Point out each leukocyte.
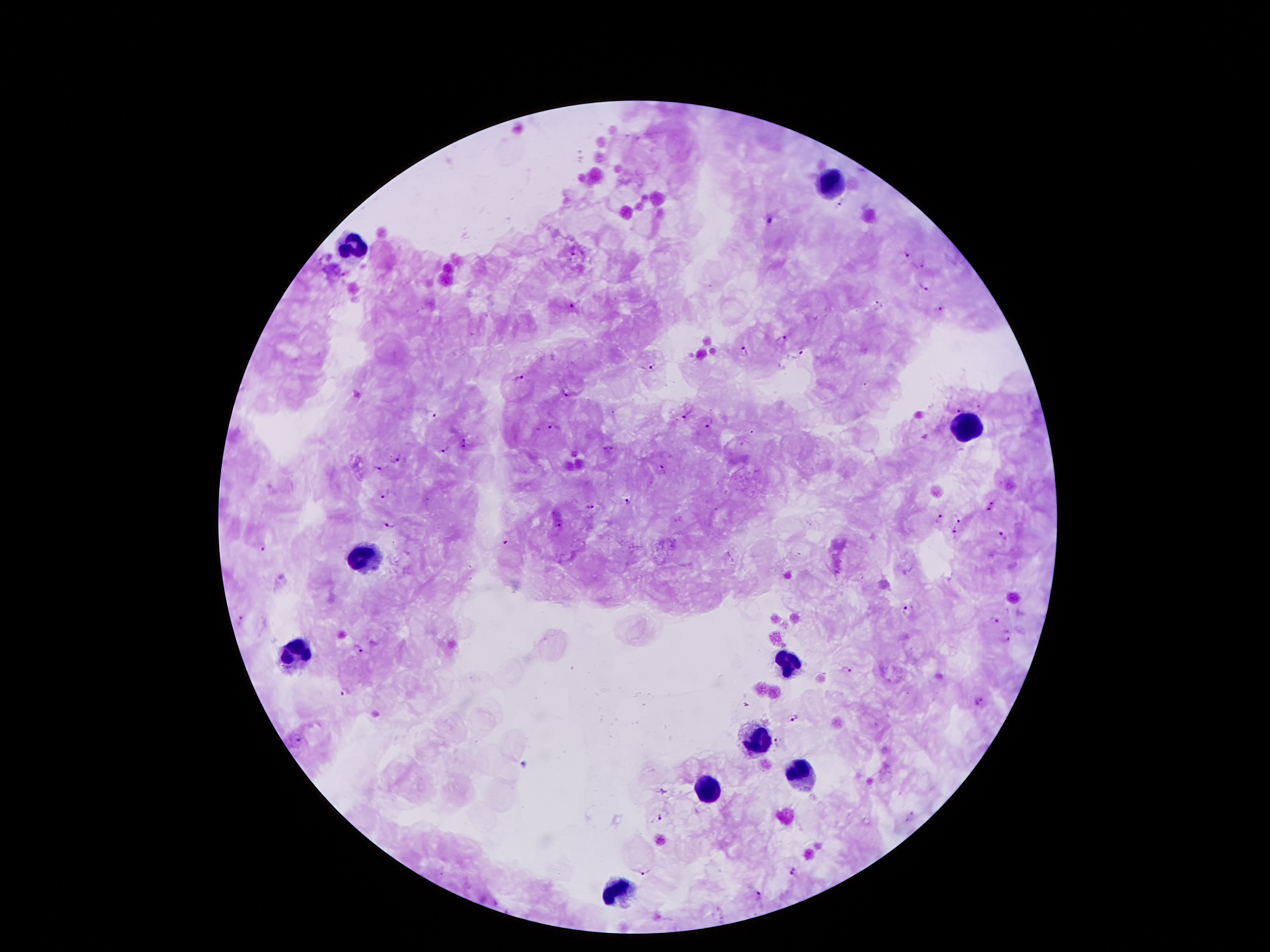
Approximate object centers, in pixels from the top-left corner.
Leukocytes: (x=830, y=181), (x=347, y=246), (x=965, y=425), (x=362, y=557), (x=297, y=656), (x=792, y=664), (x=757, y=740), (x=803, y=773), (x=706, y=788), (x=618, y=891).

Malaria parasite locations: (x=840, y=203), (x=771, y=219), (x=572, y=253), (x=905, y=255), (x=917, y=264), (x=921, y=286), (x=572, y=305), (x=879, y=305), (x=939, y=309), (x=781, y=339), (x=802, y=352), (x=746, y=353), (x=652, y=365), (x=518, y=377), (x=566, y=393), (x=960, y=409), (x=431, y=414), (x=683, y=414), (x=709, y=423), (x=550, y=427), (x=465, y=442), (x=608, y=448), (x=447, y=449), (x=395, y=459), (x=378, y=468), (x=662, y=470), (x=385, y=495), (x=628, y=499), (x=590, y=507), (x=991, y=507), (x=957, y=518), (x=941, y=520), (x=391, y=524), (x=556, y=524), (x=954, y=530), (x=1002, y=535), (x=504, y=539), (x=261, y=546), (x=907, y=610), (x=242, y=620), (x=994, y=620), (x=1005, y=638), (x=357, y=648), (x=846, y=670), (x=345, y=691), (x=979, y=701), (x=796, y=717), (x=298, y=735), (x=776, y=742), (x=911, y=814), (x=659, y=816), (x=792, y=869), (x=646, y=872), (x=758, y=894). One field from this slide. Image is 1270×952 pixels. 100x magnification. Patient malaria status: infected with Plasmodium falciparum. Thick blood film. Giemsa-stained preparation. Photographed through the microscope eyepiece with a smartphone camera.